Report the malaria status of this cell.
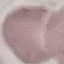

It is uninfected.

Automatically extracted cell patch, resized to 64 × 64 pixels. Photographed with a smartphone camera at the microscope eyepiece. Giemsa stain. Thin smear of blood.